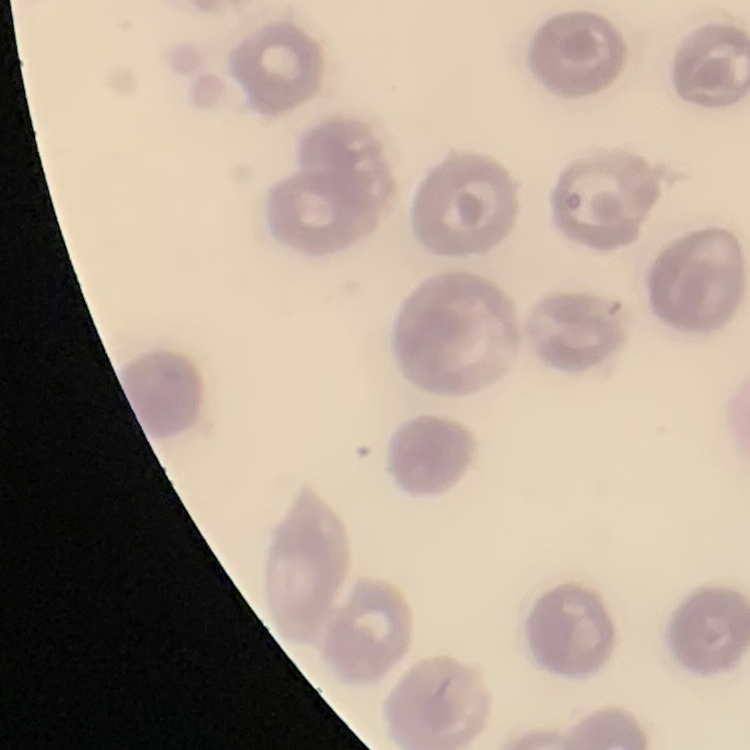
The red blood cells exhibit no rouleaux formation. Square crop of a larger photomicrograph. Thin peripheral smear. Field's or Giemsa stain.